Point out each malaria parasite.
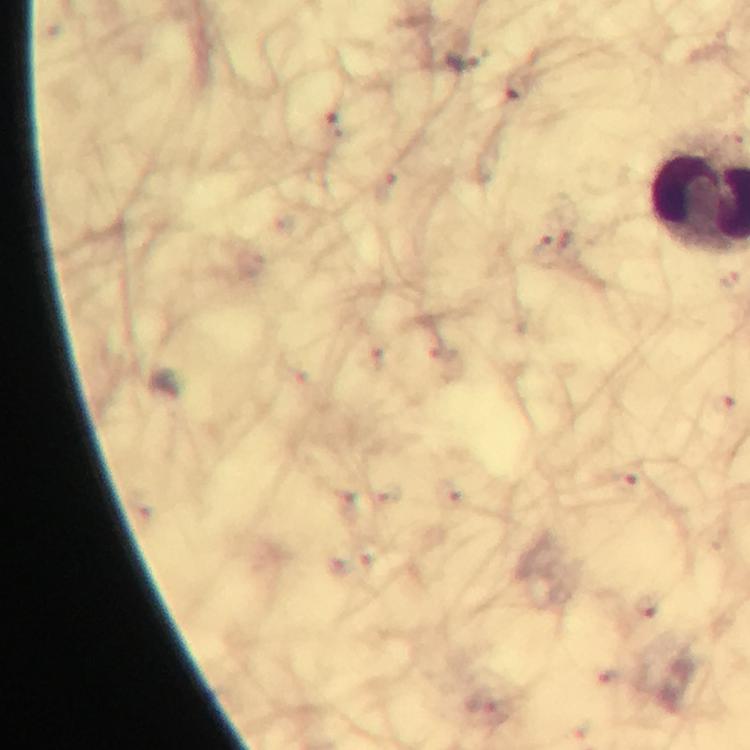

Approximate centers as [x, y] in pixels.
Malaria parasites: [515, 86], [333, 123], [624, 483], [645, 606].

Summary:
  - Context: from a diagnostic examination for malaria
  - Capture: smartphone camera through the microscope
  - Magnification: 100x
  - Image size: 750×750 pixels
  - Cropped from: a single field of view
  - Stain: Giemsa
  - Immersion oil: used
  - Preparation: thick blood smear